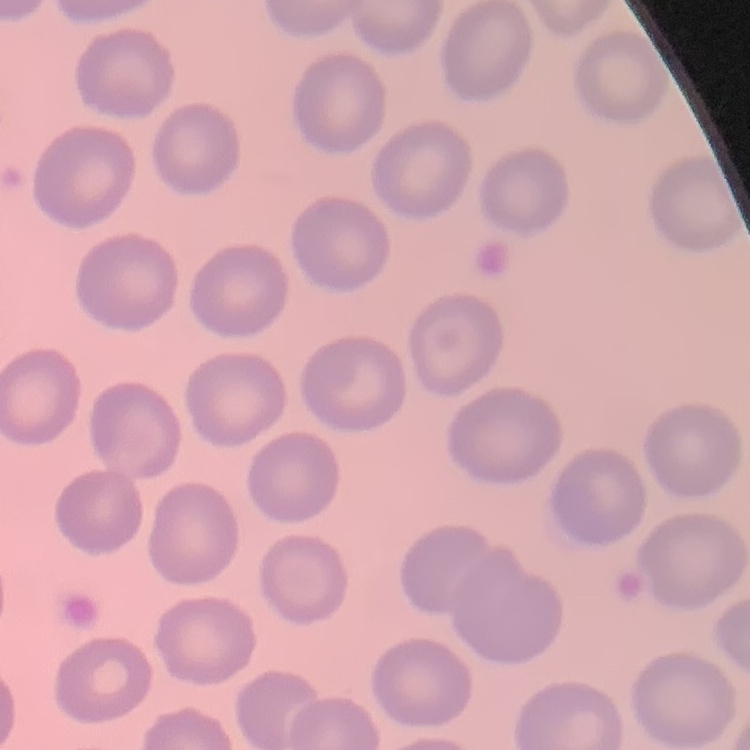

erythrocyte morphology = no rouleaux formation
image type = one tile cut from a larger photomicrograph
preparation = thin peripheral smear
stain = Field's or Giemsa